Outline each Babesia divergens-infected red blood cell.
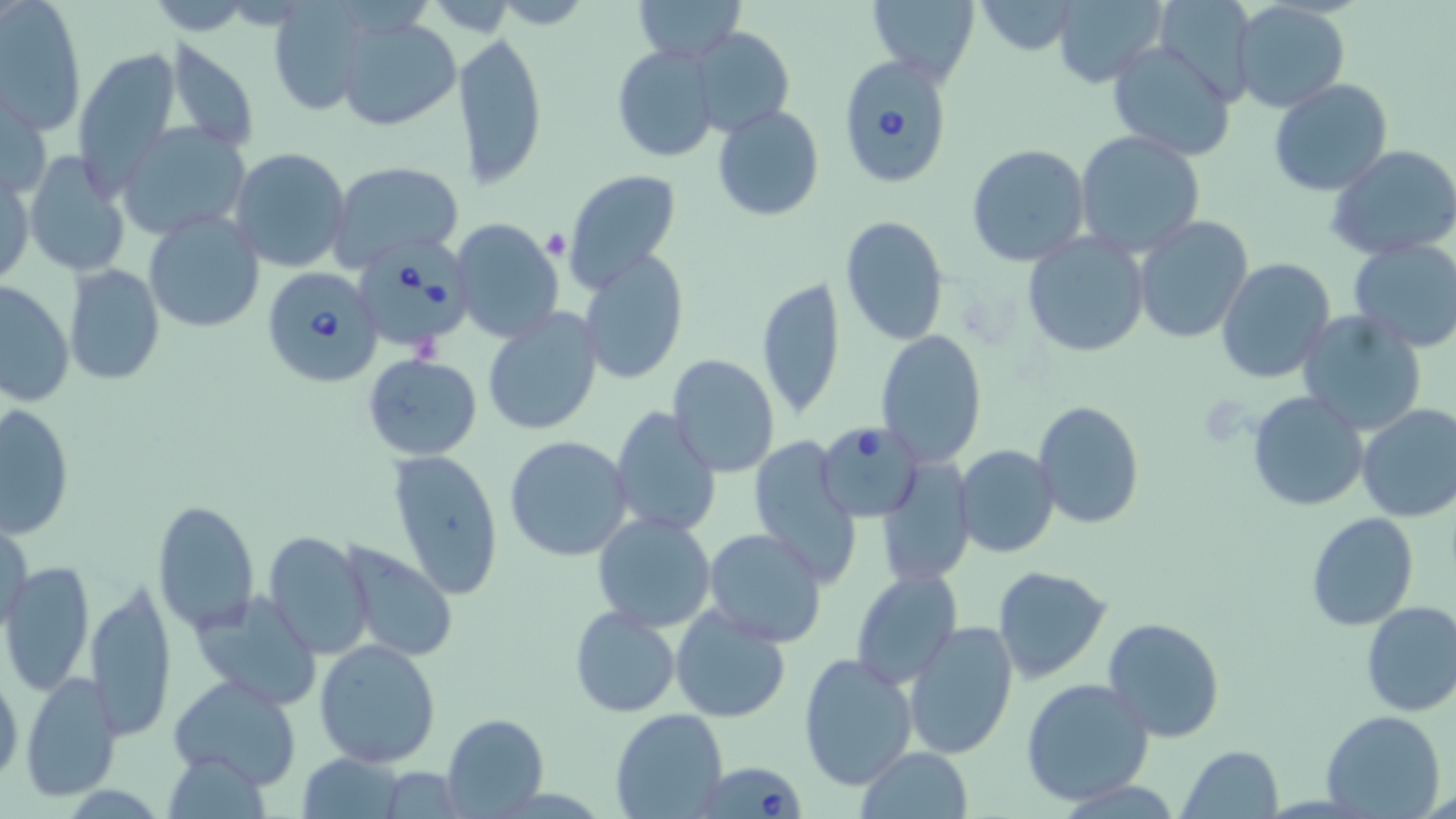
Approximate bounding boxes as [x1, y1, x2, y2] in pixels.
Babesia divergens-infected red blood cells: [839, 57, 955, 191], [352, 241, 475, 353], [263, 267, 383, 389], [818, 423, 924, 522], [695, 758, 809, 819].

slide-level diagnosis = Babesia divergens
modality = light microscopy
preparation = thin blood smear
uninfected red blood cell locations = approximate bounding boxes as [x1, y1, x2, y2] in pixels: [633, 0, 747, 61], [866, 0, 981, 85], [1051, 0, 1168, 88], [2, 1, 85, 135], [975, 1, 1079, 55], [1148, 1, 1258, 105], [265, 3, 378, 116], [1230, 3, 1351, 114], [333, 13, 461, 132], [691, 28, 794, 137], [452, 32, 547, 187], [1106, 38, 1238, 159], [163, 40, 259, 153], [610, 42, 721, 163], [72, 47, 181, 195], [1268, 78, 1394, 196], [1, 80, 49, 203], [712, 105, 824, 221], [116, 122, 249, 238], [1074, 130, 1206, 257], [967, 143, 1091, 266], [1327, 143, 1456, 261], [229, 148, 352, 273], [24, 153, 129, 276], [326, 161, 464, 273], [1, 164, 34, 290], [563, 169, 682, 290], [143, 211, 267, 334], [838, 216, 950, 346], [1135, 216, 1253, 342], [449, 219, 564, 344], [1021, 232, 1150, 358], [1347, 239, 1456, 352], [579, 249, 689, 383], [1215, 257, 1337, 382], [65, 265, 166, 385], [758, 276, 844, 420], [0, 282, 72, 409], [481, 306, 602, 437], [1297, 310, 1427, 434], [875, 330, 990, 467], [362, 354, 482, 460], [667, 356, 780, 478], [1245, 391, 1368, 512], [1032, 400, 1144, 531], [2, 402, 75, 537], [1356, 402, 1456, 523], [609, 405, 721, 537], [504, 435, 633, 562], [750, 435, 863, 588], [954, 444, 1059, 560], [389, 451, 503, 600], [874, 459, 974, 586], [153, 500, 259, 632], [1306, 511, 1420, 632], [592, 513, 717, 633], [1, 516, 34, 635], [704, 527, 827, 648], [264, 532, 373, 660], [343, 545, 456, 661], [1, 562, 94, 698], [989, 565, 1112, 684], [849, 569, 961, 691], [86, 580, 175, 740], [188, 590, 323, 709], [1358, 600, 1456, 717], [669, 601, 793, 724], [570, 607, 680, 717], [1102, 616, 1226, 742], [903, 619, 1019, 760], [314, 638, 443, 769], [797, 652, 919, 791], [0, 664, 23, 792], [19, 672, 122, 802], [168, 674, 304, 788], [1021, 677, 1154, 807], [609, 709, 727, 819], [1321, 710, 1445, 819], [442, 713, 548, 818], [1180, 745, 1284, 819], [857, 746, 973, 819], [297, 754, 407, 818]
field of view = one of a larger specimen
platelet locations = approximate bounding boxes as [x1, y1, x2, y2] in pixels: [542, 229, 571, 260], [1198, 400, 1251, 446]
stain = May-Grünwald-Giemsa
image size = 1456×819 pixels
magnification = 1000x